Point out each Plasmodium parasite.
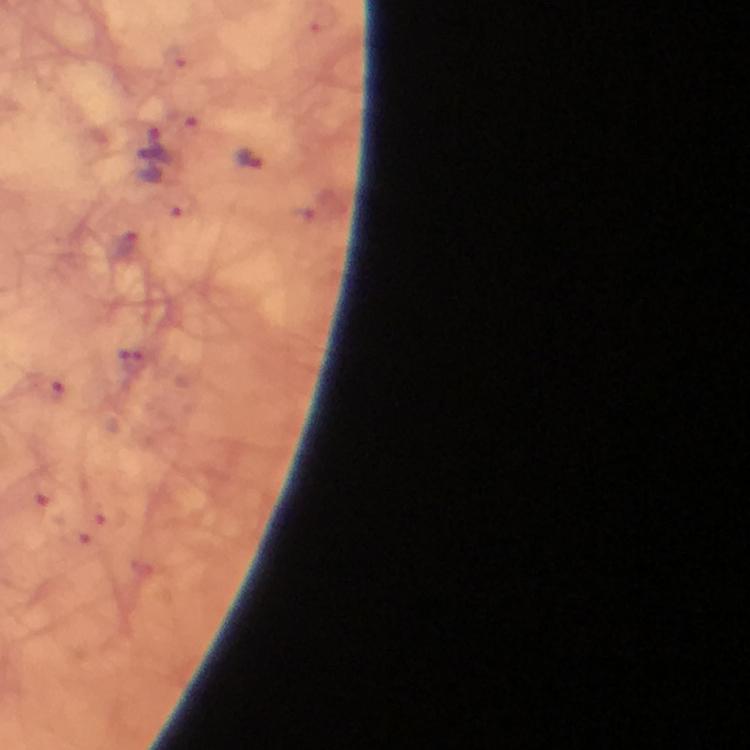

Approximate centers as (x, y) in pixels.
Plasmodium parasites: (152, 147), (250, 158), (131, 357).

magnification = 100x
preparation = thick blood film
cropped from = a single field of view
image size = 750×750 pixels
context = from a diagnostic examination for malaria
capture = smartphone mounted on the microscope
immersion oil = applied
stain = Giemsa